Name the parasite shown.
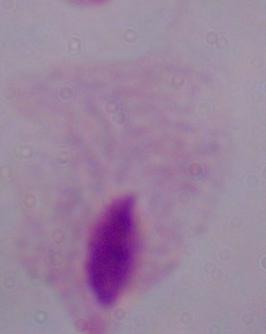

This is a trichomonad.

Photomicrograph. Captured at 1000x magnification.